Assess the morphology of the red blood cells.
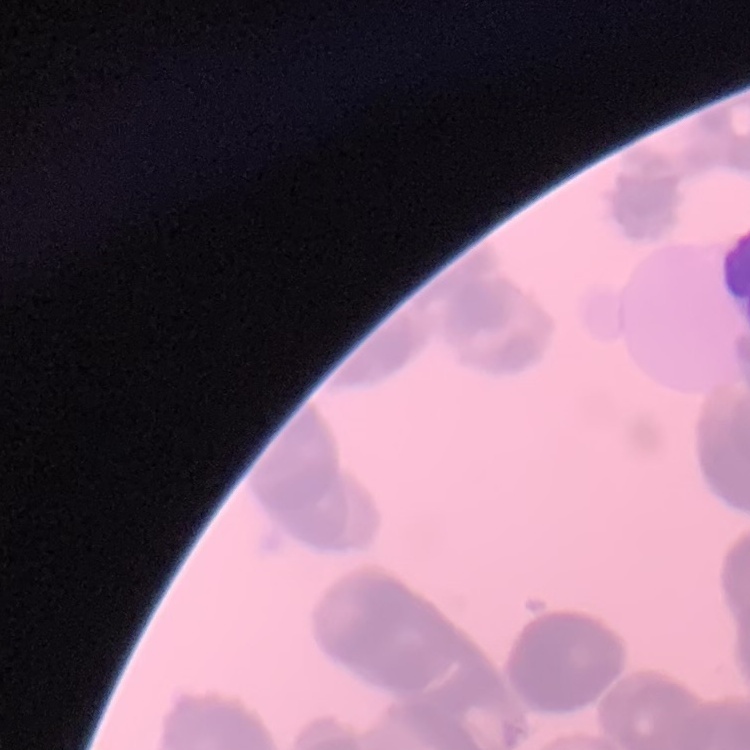
Rouleaux formation.

Summary:
  - Stain: Field's or Giemsa
  - Image type: one tile cut from a larger photomicrograph
  - Preparation: thin peripheral smear